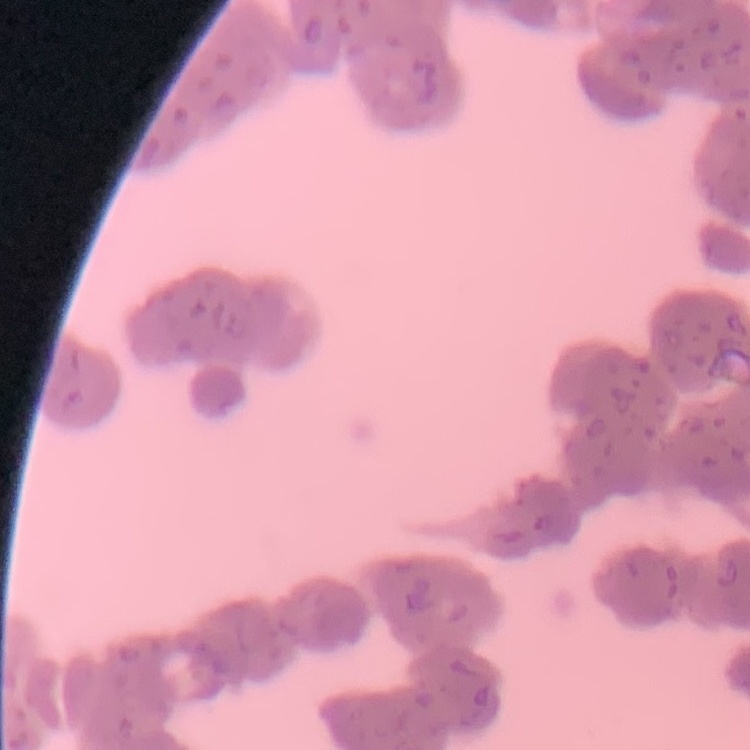
The erythrocytes exhibit rouleaux formation. Stained with either Field's or Giemsa. One tile cut from a larger photomicrograph. Thin blood smear.